Classify this cell by malaria status.
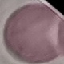

Uninfected.

Photographed with a smartphone camera at the microscope eyepiece. Thin blood smear. Automatically extracted cell patch, resized to 64 × 64 pixels. Giemsa-stained preparation.